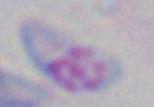

Summary:
  - Magnification: 1000x
  - Modality: photomicrograph
  - Identification: Toxoplasma gondii